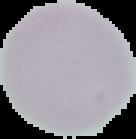
Summary:
  - Result: negative for Plasmodium parasites
  - Image size: 136×139 pixels
  - Preparation: thin blood film
  - Image type: segmented cell region on a black background